Outline each Plasmodium ovale-infected red blood cell.
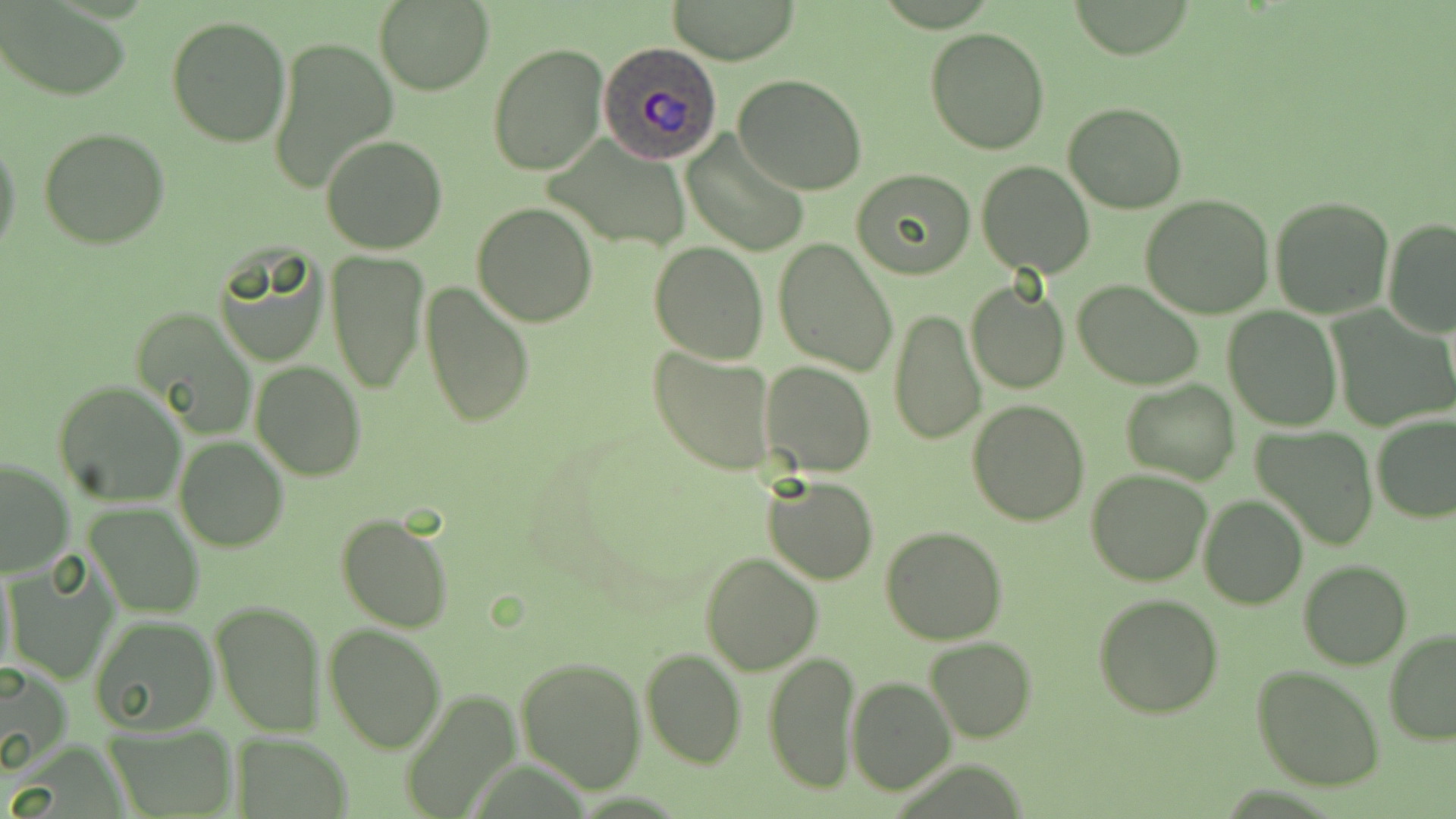

Approximate bounding boxes as (x1,y1)-(x2,y2) corner pairs in pixels.
Plasmodium ovale-infected red blood cells: (598,42)-(724,165).

Summary:
  - Uninfected red blood cell locations: (666,0)-(802,66), (1067,0)-(1199,59), (374,1)-(494,95), (2,3)-(131,101), (166,13)-(292,148), (925,27)-(1051,155), (266,33)-(398,195), (487,42)-(608,176), (733,74)-(868,195), (1062,103)-(1189,215), (38,126)-(169,249), (681,131)-(810,256), (0,134)-(23,262), (321,134)-(447,255), (545,139)-(689,253), (976,160)-(1094,279), (851,168)-(976,279), (1142,195)-(1274,318), (1270,195)-(1396,319), (472,202)-(598,327), (1382,216)-(1456,337), (772,238)-(898,376), (649,241)-(768,363), (214,248)-(330,367), (327,250)-(429,393), (1074,280)-(1204,388), (422,281)-(534,429), (966,283)-(1068,395), (133,307)-(258,440), (1224,307)-(1341,430), (887,309)-(986,447), (1330,309)-(1455,432), (649,345)-(777,475), (251,360)-(366,481), (759,360)-(875,477), (53,378)-(188,507), (1120,378)-(1239,486), (968,399)-(1089,524), (1371,413)-(1456,523), (1254,427)-(1378,551), (174,435)-(289,551), (0,458)-(74,576), (1087,469)-(1213,586), (761,474)-(881,585), (1198,496)-(1306,610), (85,502)-(202,618), (335,512)-(454,634), (879,528)-(1007,645), (699,553)-(823,676), (3,556)-(120,685), (1299,561)-(1411,669), (1093,594)-(1224,718), (208,599)-(325,738), (211,611)-(445,743), (88,614)-(219,736), (325,623)-(448,753), (1384,629)-(1456,744), (925,636)-(1036,742), (641,647)-(747,768), (516,655)-(647,793), (762,656)-(860,793), (1,660)-(73,774), (1253,665)-(1387,791), (846,674)-(956,795), (396,687)-(518,816), (100,722)-(239,817), (234,732)-(355,818)
  - Slide-level diagnosis: Plasmodium ovale
  - Modality: light microscopy
  - Field of view: single
  - Stain: May-Grünwald-Giemsa
  - Magnification: 1000x
  - Image size: 1456×819 pixels
  - Preparation: thin blood film